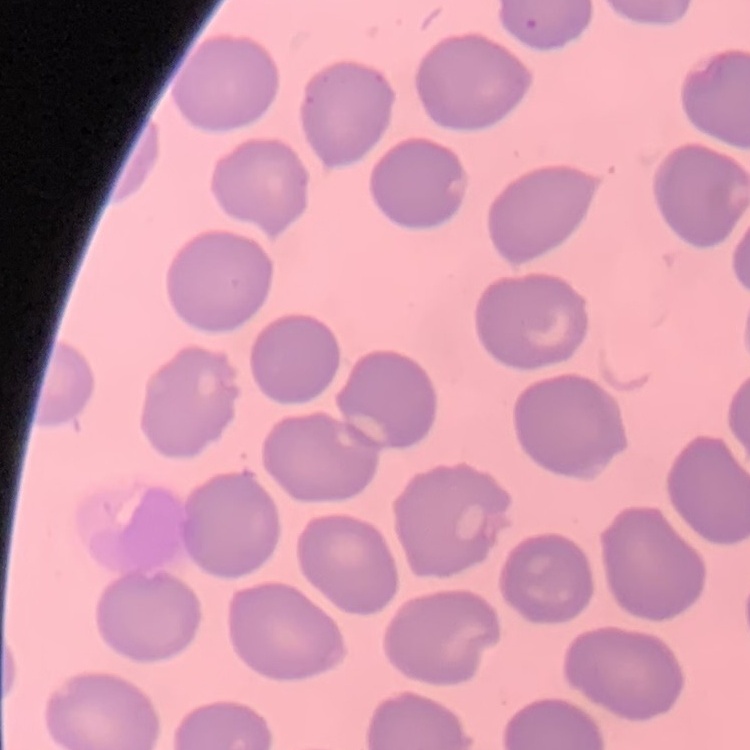
red blood cell morphology = no rouleaux formation
stain = Field's or Giemsa
preparation = thin blood film
image type = one tile cut from a larger photomicrograph